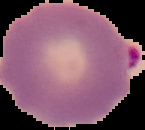
From a thin blood smear. Malaria status: parasitized. Cell region segmented out of the field of view; the surrounding area is masked to black. Image is 145×130 pixels.